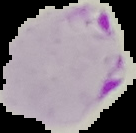

Summary:
  - Image type: segmented cell region on a black background
  - Preparation: thin blood smear
  - Malaria status: parasitized
  - Image size: 136×133 pixels